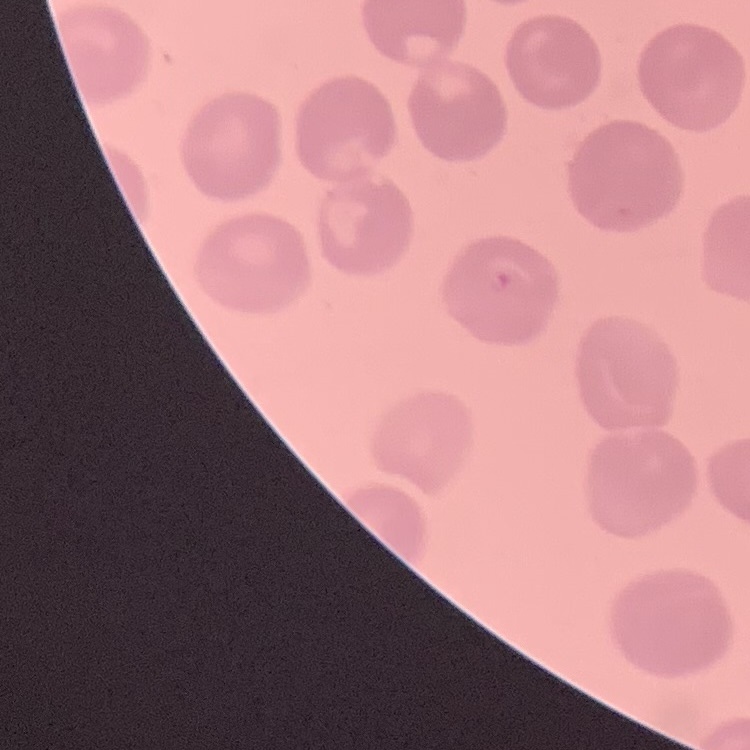
Summary:
  - Red blood cell morphology: no rouleaux formation
  - Preparation: thin blood film
  - Stain: Field's or Giemsa
  - Image type: square crop of a larger photomicrograph